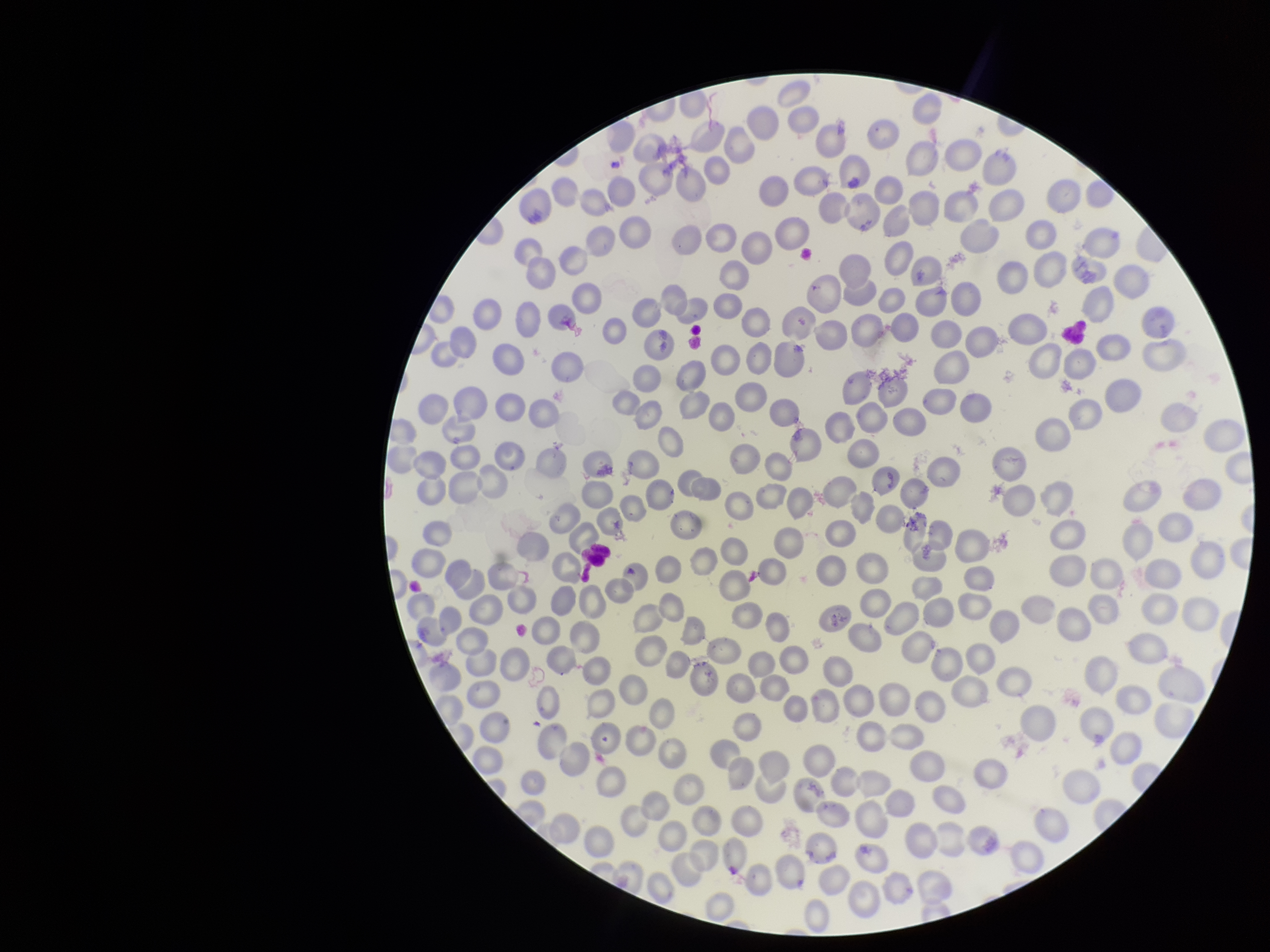

Summary:
  - Image size: 1270×952 pixels
  - Parasitized red blood cells: none seen
  - Red blood cell count: 267
  - Field of view: one from this slide
  - Preparation: thin smear
  - Capture: smartphone photograph through the microscope eyepiece
  - Species reported for this patient: Plasmodium falciparum
  - Stain: Giemsa
  - Patient malaria status: positive
  - Parasitized red blood cell count: 0